Identify the parasite.
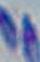

This is Toxoplasma gondii.

Summary:
  - Magnification: 1000x
  - Modality: micrograph